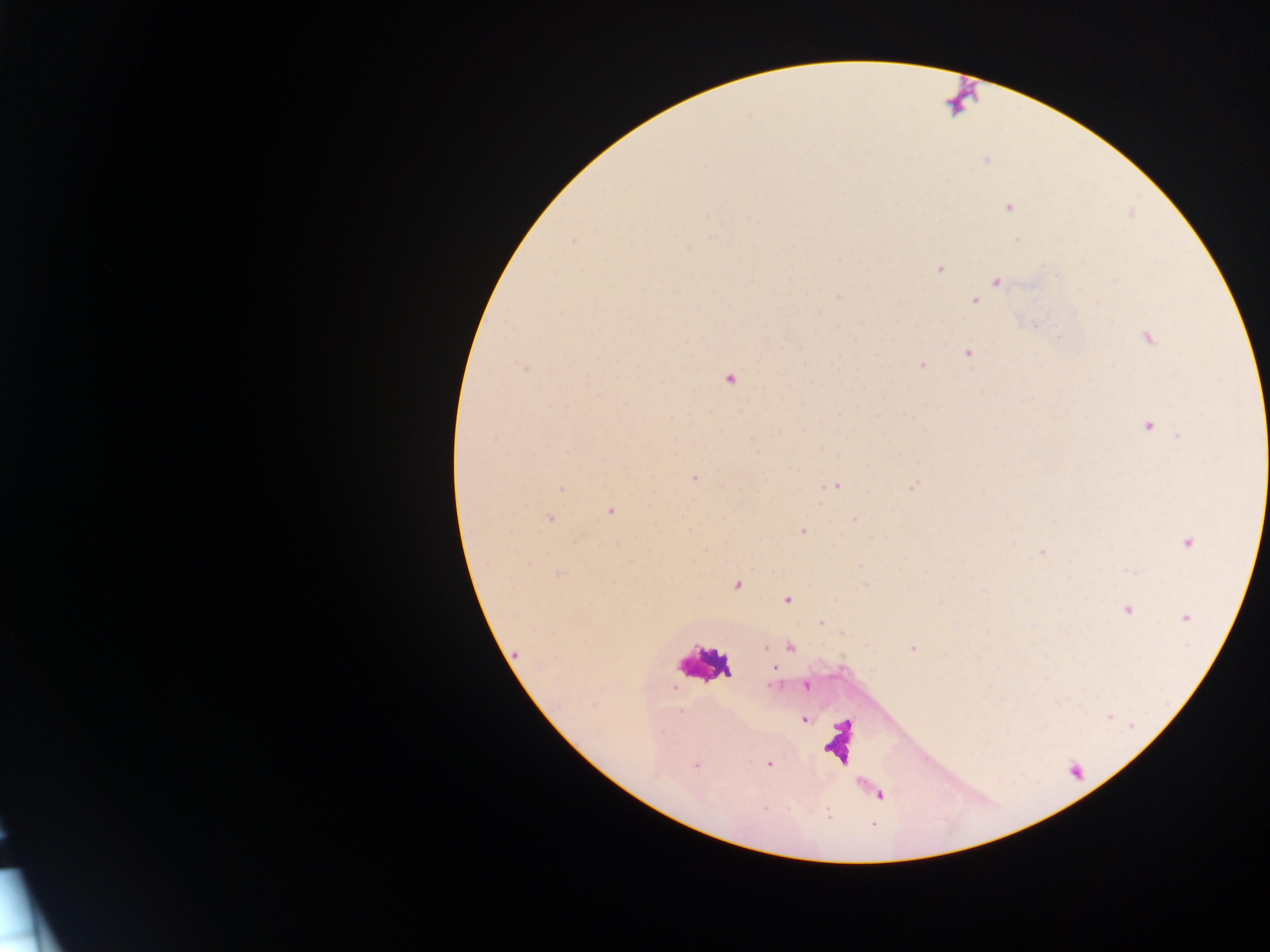
capture = mobile-phone photograph through a microscope
field of view = single
preparation = thick blood smear
image size = 1270×952 pixels
leukocyte locations = approximate centers as (x, y) in pixels: (709, 660), (842, 740)
Plasmodium parasite locations = approximate centers as (x, y) in pixels: (985, 160), (1009, 207), (710, 215), (711, 238), (1018, 239), (573, 240), (939, 270), (997, 282), (976, 300), (1035, 326), (1148, 338), (968, 353), (921, 366), (525, 368), (730, 379), (565, 406), (1147, 427), (694, 477), (836, 486), (913, 486), (561, 489), (610, 512), (550, 518), (803, 531), (1188, 542), (1042, 552), (559, 573), (737, 584), (787, 599), (1127, 610), (1186, 618), (821, 622), (765, 647), (790, 647), (913, 648), (774, 669), (771, 685), (806, 685), (681, 712), (1109, 717), (804, 720), (769, 764), (697, 765), (765, 807), (828, 814)
country = Ghana